State which parasite is depicted.
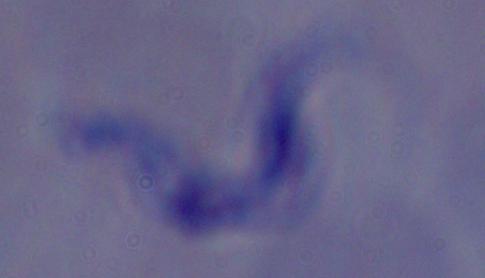

A trypanosome.

modality = photomicrograph
magnification = 1000x